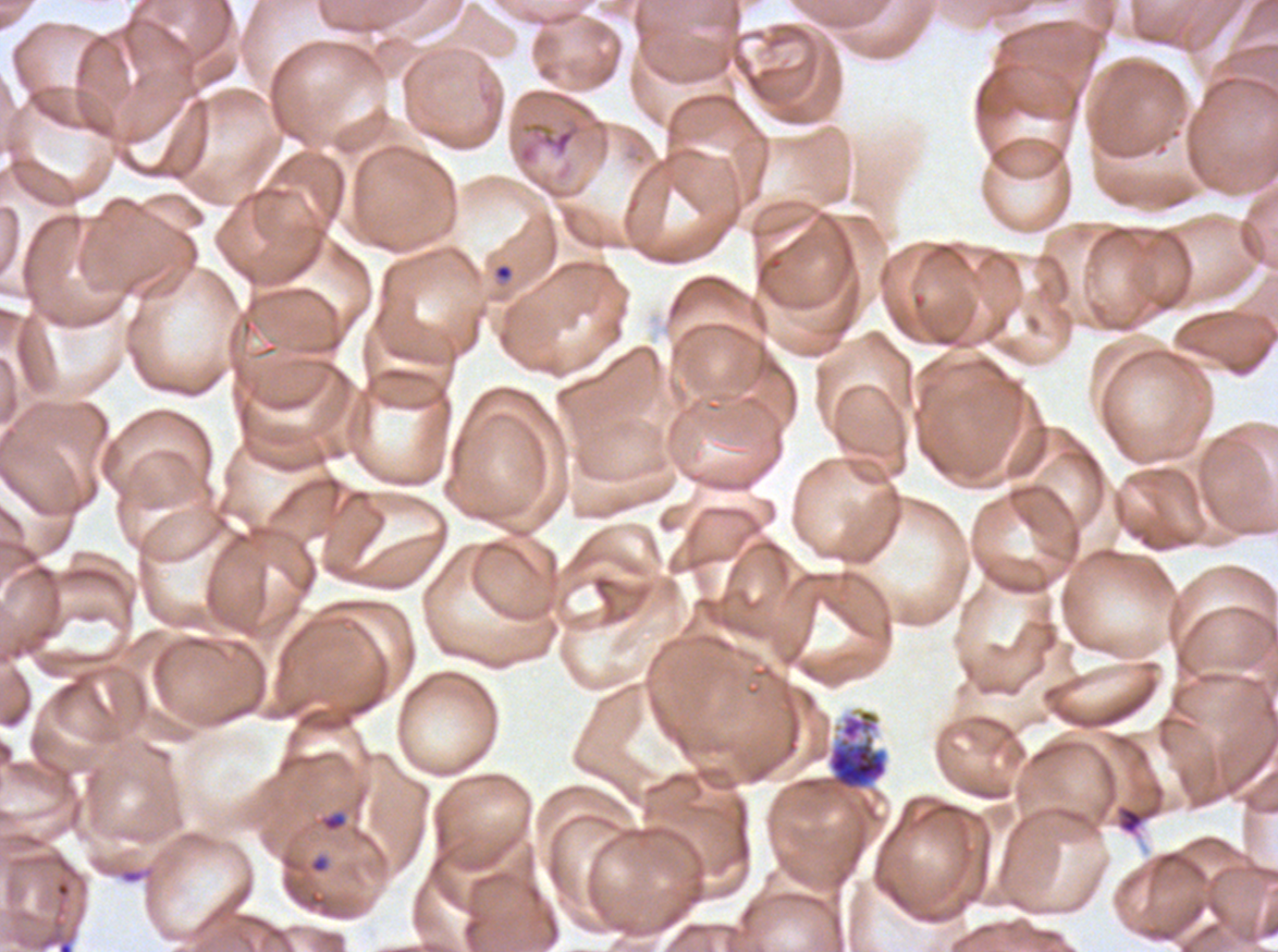
Approximate bounding boxes as (x1, y1, x2, y2) in pixels.
Summary:
  - Debris locations: (516, 116, 584, 166), (1115, 803, 1160, 836)
  - Segmenter locations: (827, 708, 888, 791)
  - Ring locations: (493, 262, 514, 282), (321, 811, 348, 833)
  - Image size: 1278×952 pixels
  - Stain: Giemsa
  - Specimen: Plasmodium falciparum from a patient in The Gambia, cultured ex vivo for 24 to 48 hours
  - Preparation: thin blood film
  - Field of view: sub-image separated from a larger composite
  - Life-cycle stages observed: ring, segmenter